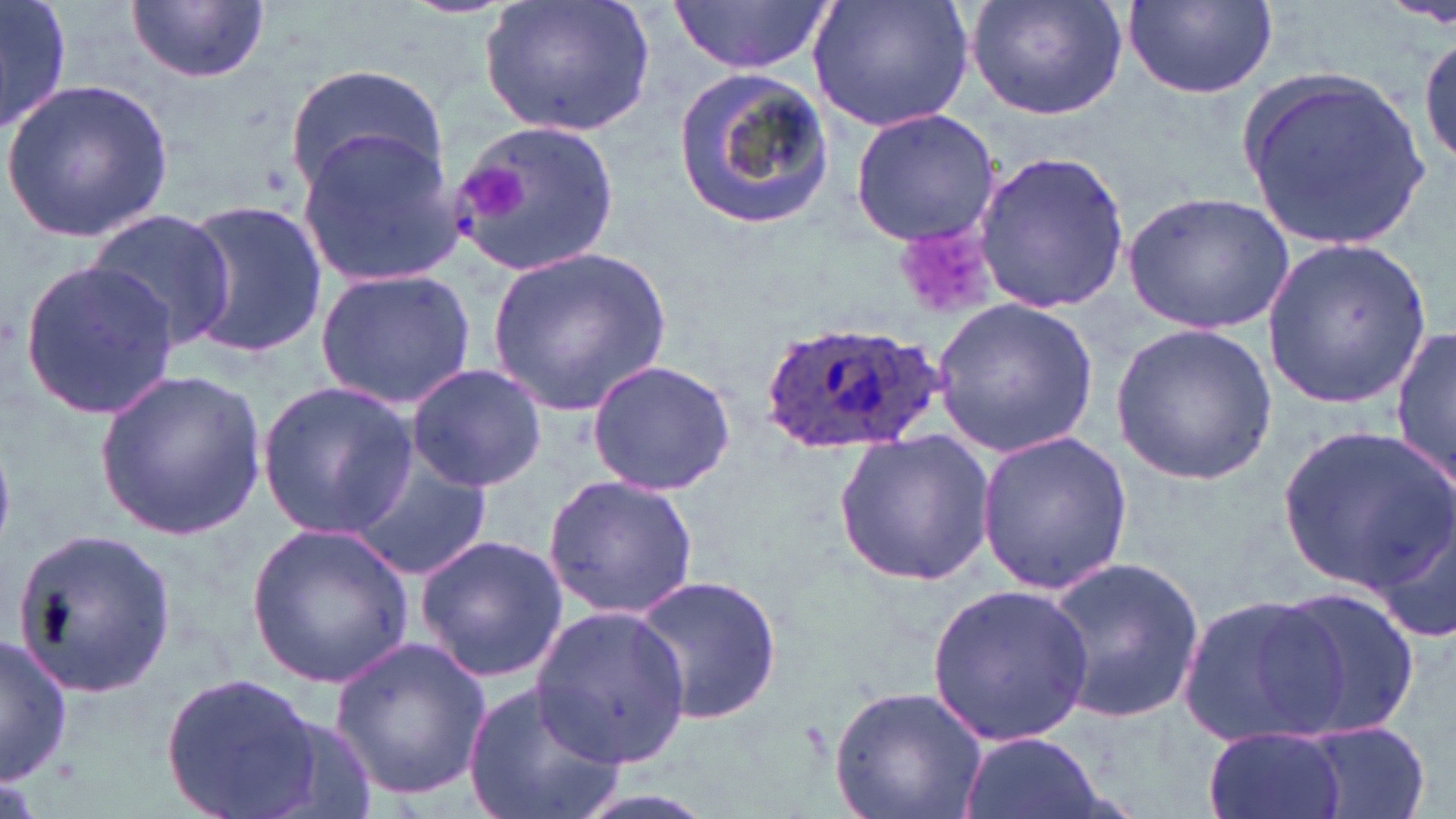 Approximate bounding boxes as (x1,y1)-(x2,y2) corner pairs in pixels. Uninfected red blood cell locations: (0,0)-(70,138), (479,0)-(658,137), (670,0)-(834,75), (807,0)-(974,132), (965,0)-(1128,121), (1121,0)-(1280,101), (126,2)-(270,85), (1416,32)-(1456,171), (674,61)-(837,232), (286,64)-(447,196), (1232,67)-(1431,248), (3,78)-(173,243), (848,108)-(1002,246), (451,122)-(622,277), (295,134)-(459,285), (972,147)-(1133,316), (1122,189)-(1296,336), (175,197)-(329,361), (84,209)-(236,351), (1260,236)-(1431,410), (485,244)-(675,417), (19,256)-(180,423), (315,268)-(477,411), (931,296)-(1100,459), (1107,321)-(1281,485), (1392,324)-(1455,490), (585,359)-(737,495), (406,363)-(548,492), (94,367)-(266,541), (256,381)-(416,539), (1280,426)-(1454,590), (975,428)-(1133,596), (834,432)-(997,588), (347,448)-(492,581), (543,474)-(701,619), (1366,500)-(1456,645), (245,523)-(415,687), (11,528)-(180,701), (413,531)-(571,685), (1045,554)-(1205,729), (634,569)-(785,725), (925,581)-(1096,744), (1265,586)-(1421,739), (1175,590)-(1346,751), (532,602)-(693,763), (329,632)-(492,803), (0,635)-(73,787), (159,672)-(323,818), (463,677)-(627,819), (829,683)-(991,819), (247,710)-(380,819), (1297,723)-(1434,818), (1203,726)-(1351,819), (958,730)-(1105,819). Plasmodium ovale-infected red blood cell locations: (763,314)-(937,452). Platelet locations: (463,166)-(527,221), (900,230)-(995,322). Slide-level diagnosis: Plasmodium ovale. Thin blood film. One field of a larger specimen. Captured at 1000x magnification. Image is 1456×819 pixels. May-Grünwald-Giemsa stain. Light microscopy.